State which parasite is depicted.
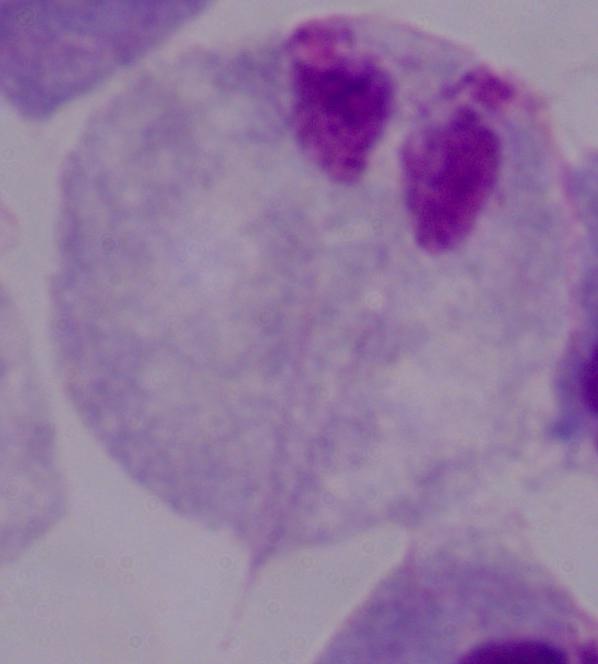
A trichomonad.

Summary:
  - Magnification: 1000x
  - Modality: photomicrograph